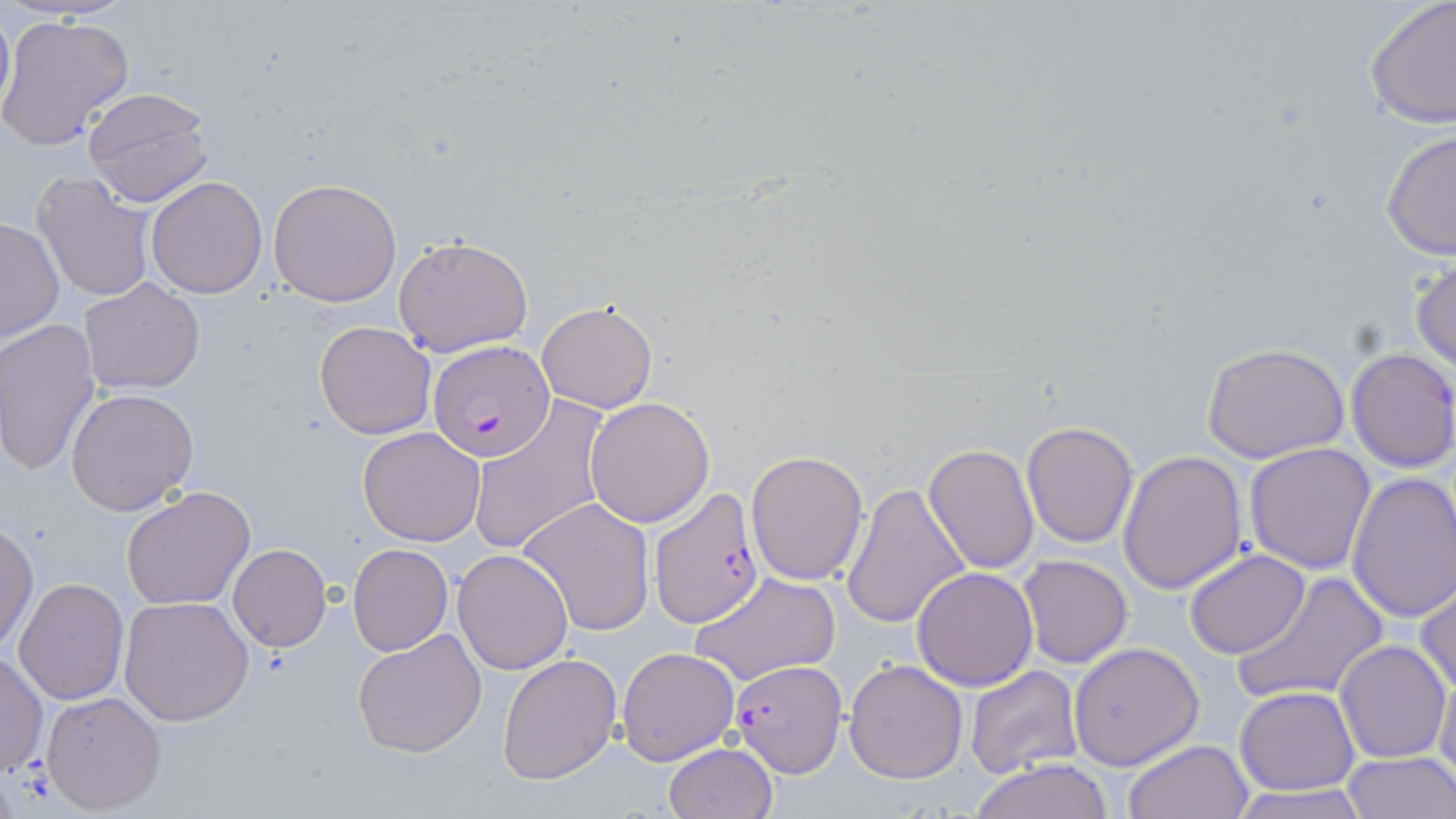

{
  "slide_level_diagnosis": "Plasmodium falciparum",
  "preparation": "thin blood smear",
  "field_of_view": "single",
  "image_size": "1456×819 pixels",
  "modality": "light microscopy",
  "stain": "May-Grünwald-Giemsa",
  "uninfected_red_blood_cell_locations": "approximate bounding boxes as [x1, y1, x2, y2] in pixels: [1363, 0, 1455, 131], [0, 2, 14, 125], [0, 14, 135, 154], [82, 86, 214, 208], [1380, 128, 1456, 261], [31, 170, 158, 303], [146, 176, 269, 298], [268, 177, 402, 306], [0, 217, 64, 343], [394, 235, 535, 356], [1410, 256, 1456, 375], [78, 278, 206, 395], [537, 299, 659, 414], [0, 319, 102, 478], [313, 320, 437, 439], [1201, 342, 1352, 464], [1345, 347, 1456, 472], [66, 388, 200, 516], [585, 396, 715, 527], [467, 398, 612, 553], [1021, 420, 1139, 549], [357, 426, 486, 546], [921, 443, 1038, 575], [1244, 443, 1376, 575], [746, 449, 869, 584], [1118, 450, 1248, 594], [1346, 471, 1456, 623], [839, 482, 971, 630], [121, 486, 257, 610], [518, 497, 656, 636], [0, 521, 37, 653], [348, 542, 454, 656], [228, 544, 331, 652], [452, 549, 573, 674], [1183, 549, 1310, 660], [1017, 554, 1132, 668], [912, 567, 1039, 691], [1233, 570, 1389, 706], [689, 572, 843, 687], [13, 576, 128, 704], [1414, 579, 1456, 698], [119, 594, 255, 726], [353, 627, 487, 757], [1335, 640, 1451, 764], [1069, 642, 1204, 770], [616, 647, 740, 765], [1, 650, 47, 782], [496, 652, 622, 785], [843, 659, 968, 783], [1433, 662, 1456, 791], [963, 664, 1083, 780], [1234, 686, 1360, 795], [41, 690, 167, 813], [1121, 738, 1253, 819], [665, 743, 777, 819], [1341, 753, 1456, 818], [969, 758, 1114, 819], [1226, 786, 1373, 819]",
  "plasmodium_falciparum_infected_red_blood_cell_locations": "approximate bounding boxes as [x1, y1, x2, y2] in pixels: [428, 342, 559, 461], [647, 488, 763, 628], [728, 658, 847, 776]",
  "magnification": "1000x"
}